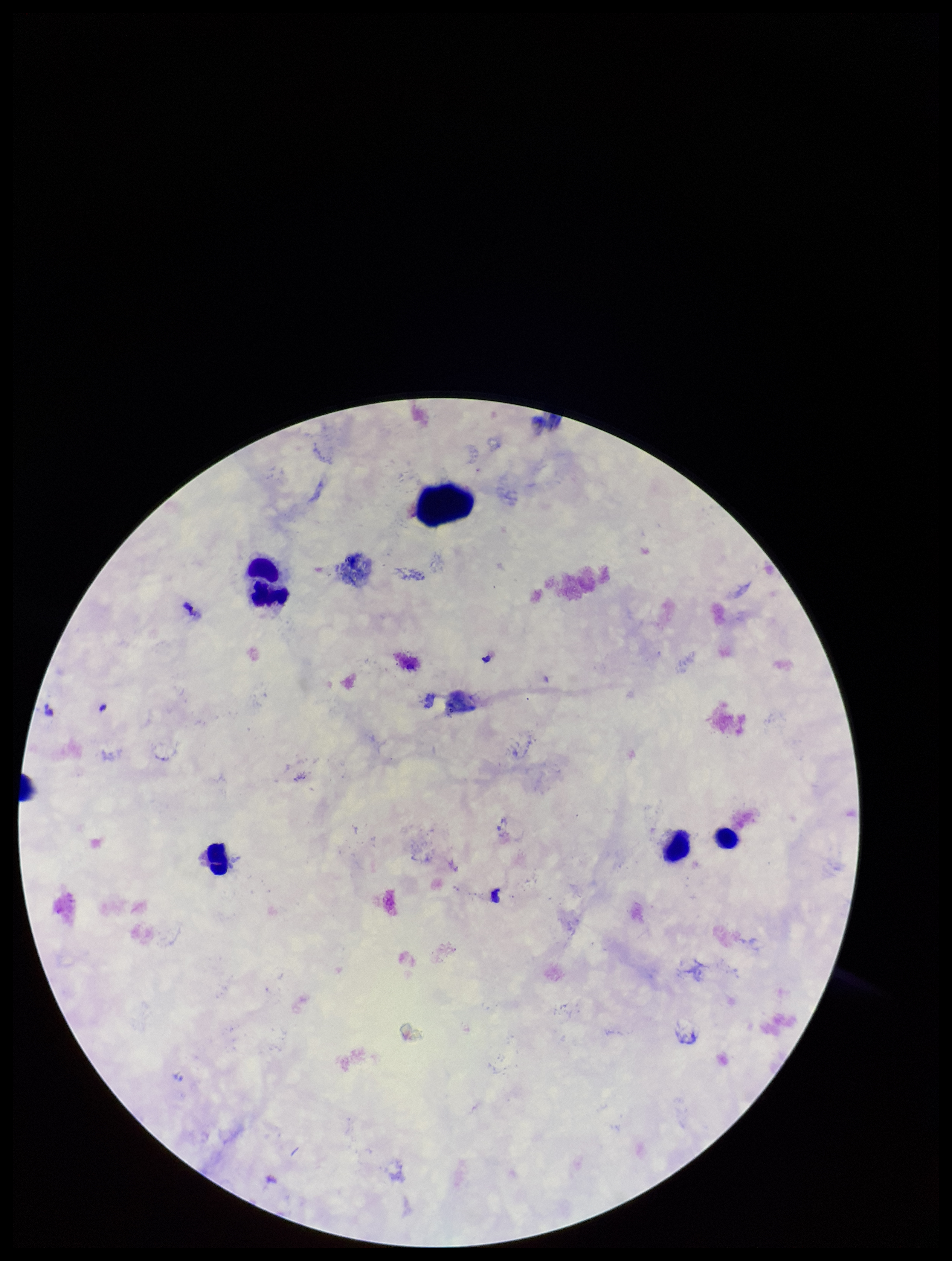

Summary:
  - Capture: smartphone photograph through the microscope eyepiece
  - Preparation: thick smear
  - Leukocyte count: 4
  - Image size: 952×1261 pixels
  - Plasmodium parasites: none seen
  - Field of view: single
  - Species reported for this patient: Plasmodium falciparum
  - Stain: Giemsa
  - Patient malaria status: positive
  - Parasite count: 0